Give the position of every Plasmodium parasite.
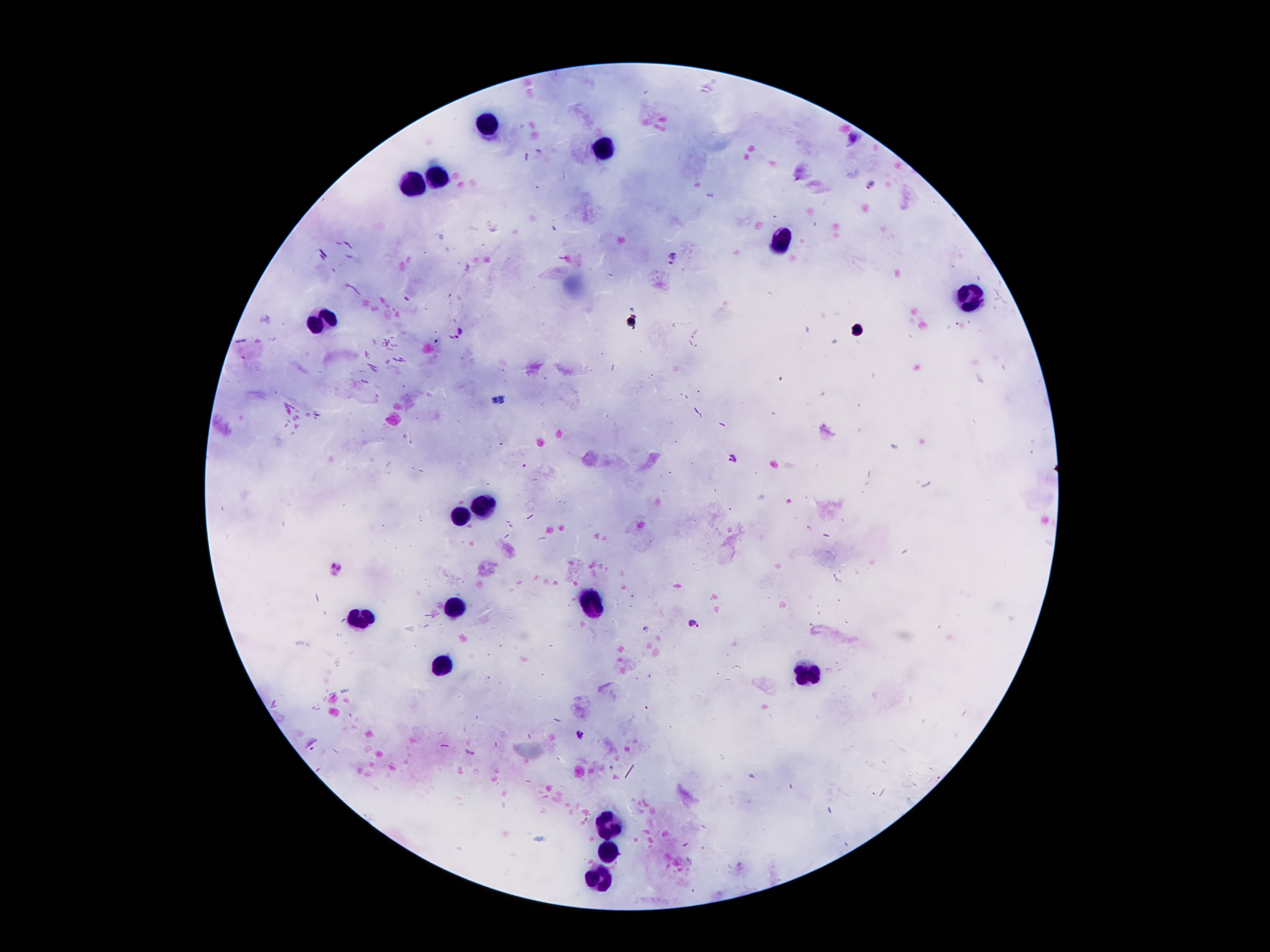
Approximate centers as [x, y] in pixels.
Plasmodium parasites: [870, 184], [673, 259], [457, 332], [732, 460], [337, 569], [695, 624], [580, 734].

leukocyte locations = [491, 121], [609, 146], [441, 174], [411, 185], [783, 239], [969, 296], [325, 319], [479, 505], [461, 514], [592, 601], [454, 609], [359, 617], [443, 666], [808, 673], [611, 825], [611, 850], [602, 876]
preparation = thick blood smear
capture = smartphone camera through the microscope eyepiece
magnification = 100x
image size = 1270×952 pixels
field of view = one from this slide
stain = Giemsa
patient malaria status = positive for Plasmodium falciparum